Classify this cell by malaria status.
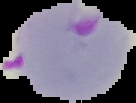
Parasitized.

From a thin blood smear. Image is 136×103 pixels. Cell region segmented out of the field of view; the surrounding area is masked to black.